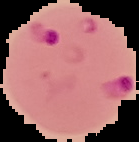
The area outside the segmented cell region is set to black. From a thin blood smear. Image is 139×142 pixels. Result: Plasmodium parasites identified.